Outline each Plasmodium ovale-infected red blood cell.
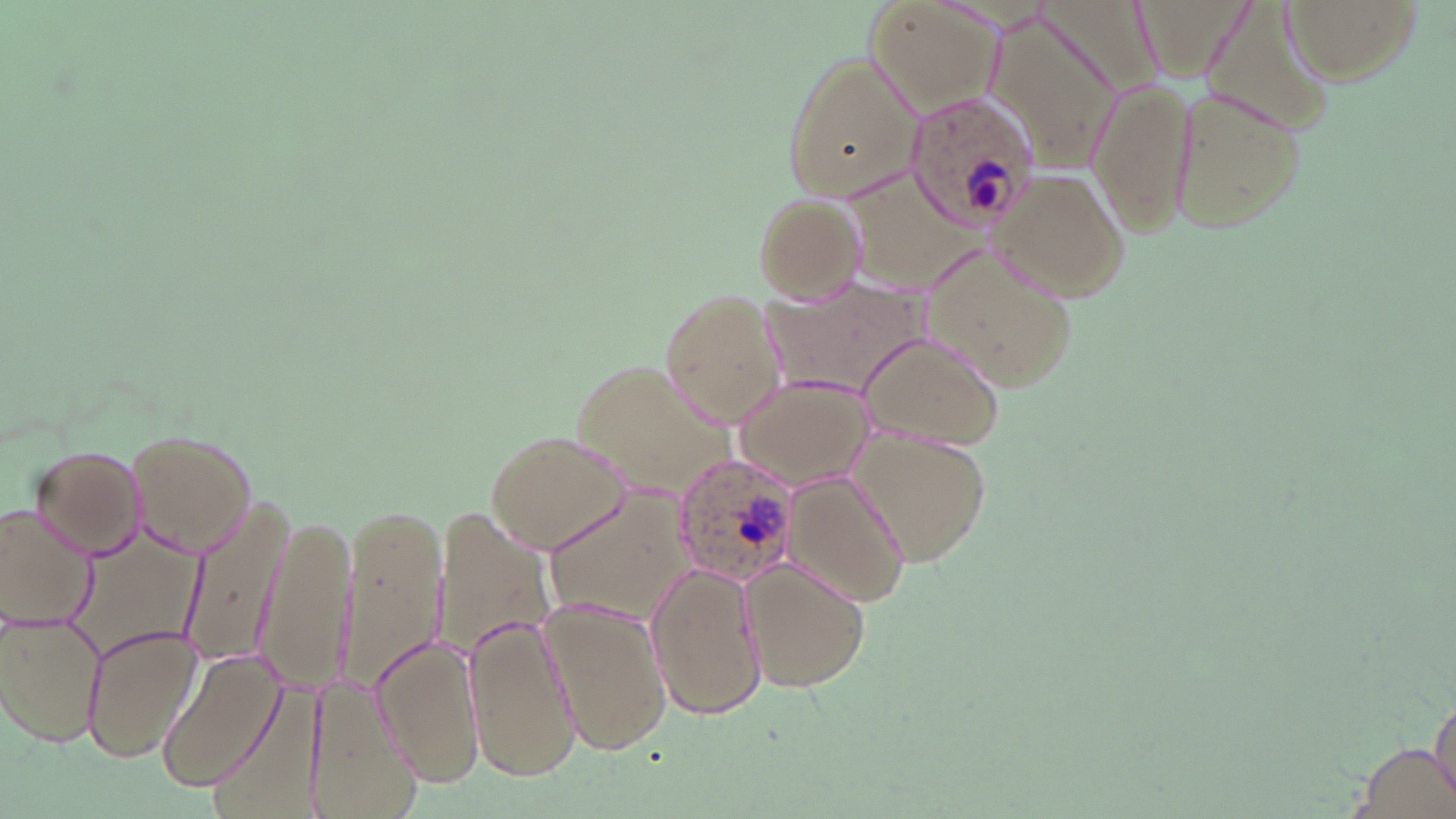

Approximate bounding boxes as [x1, y1, x2, y2] in pixels.
Plasmodium ovale-infected red blood cells: [899, 93, 1043, 233], [669, 452, 803, 586].

{
  "slide_level_diagnosis": "Plasmodium ovale",
  "field_of_view": "one of a larger specimen",
  "magnification": "1000x",
  "stain": "May-Grünwald-Giemsa",
  "image_size": "1456×819 pixels",
  "uninfected_red_blood_cell_locations": "approximate bounding boxes as [x1, y1, x2, y2] in pixels: [1028, 0, 1165, 97], [1198, 0, 1333, 140], [1282, 0, 1424, 85], [864, 1, 1005, 115], [985, 11, 1124, 178], [778, 54, 920, 199], [1082, 78, 1197, 242], [1162, 83, 1311, 235], [832, 165, 989, 309], [988, 166, 1132, 302], [752, 190, 867, 302], [916, 238, 1081, 396], [764, 280, 931, 399], [660, 289, 786, 428], [855, 330, 1006, 451], [570, 361, 736, 500], [735, 377, 875, 491], [485, 427, 632, 552], [847, 427, 995, 565], [124, 429, 259, 556], [29, 444, 146, 558], [783, 473, 911, 607], [541, 479, 700, 633], [178, 501, 289, 663], [0, 505, 95, 631], [432, 505, 557, 658], [339, 506, 447, 698], [256, 512, 358, 698], [63, 516, 217, 666], [738, 557, 871, 693], [645, 560, 767, 721], [537, 596, 671, 757], [1, 614, 103, 748], [463, 615, 581, 779], [78, 621, 200, 763], [370, 638, 486, 789], [156, 646, 288, 795], [205, 673, 332, 811], [303, 673, 420, 812], [1347, 739, 1456, 819]",
  "preparation": "thin blood smear",
  "modality": "light microscopy"
}